Outline platelets.
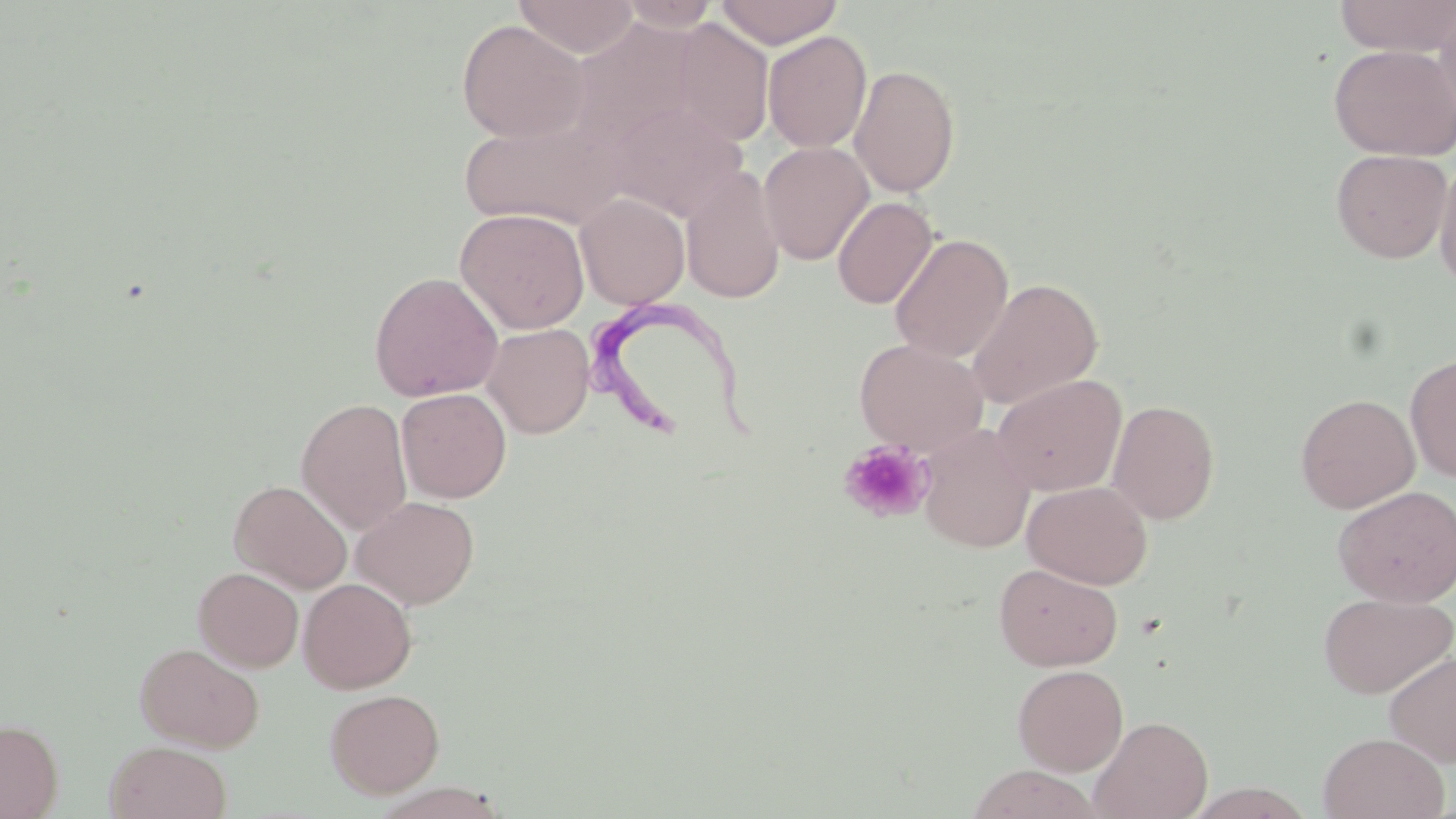

Approximate bounding boxes as (x1,y1)-(x2,y2) corner pairs in pixels.
Platelets: (838,439)-(933,523).

slide-level diagnosis = Trypanosoma brucei
uninfected red blood cell locations = approximate bounding boxes as (x1,y1)-(x2,y2) corner pairs in pixels: (512,0)-(641,58), (715,0)-(843,48), (1334,0)-(1456,57), (615,1)-(724,32), (1433,7)-(1456,126), (567,17)-(703,153), (669,18)-(774,148), (456,19)-(591,142), (763,30)-(872,153), (1328,43)-(1456,161), (849,64)-(961,197), (603,102)-(747,222), (459,113)-(625,230), (759,142)-(874,265), (1330,148)-(1452,264), (1434,155)-(1456,292), (680,165)-(785,304), (575,193)-(690,309), (832,196)-(938,309), (454,207)-(590,334), (889,233)-(1013,363), (369,271)-(503,402), (967,277)-(1104,408), (482,323)-(595,438), (854,338)-(989,454), (1405,352)-(1456,483), (992,374)-(1127,496), (396,388)-(511,503), (1296,393)-(1420,513), (296,397)-(413,534), (1107,399)-(1221,524), (917,424)-(1035,553), (229,479)-(352,593), (1022,480)-(1153,589), (1332,485)-(1456,607), (352,494)-(480,609), (993,562)-(1123,671), (193,566)-(304,672), (298,577)-(417,693), (1318,591)-(1455,699), (134,641)-(265,752), (1383,651)-(1456,767), (1012,664)-(1129,775), (324,688)-(445,798), (1089,715)-(1213,819), (0,719)-(63,818), (1317,731)-(1450,819), (104,740)-(232,819)
stain = May-Grünwald-Giemsa
image size = 1456×819 pixels
preparation = thin blood smear
field of view = single
magnification = 1000x
Trypanosoma brucei locations = approximate bounding boxes as (x1,y1)-(x2,y2) corner pairs in pixels: (582,299)-(756,452)
modality = light microscopy